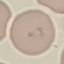
Summary:
  - Malaria status: uninfected
  - Preparation: thin smear
  - Capture: smartphone through the microscope eyepiece
  - Image type: cell patch, automatically extracted from a larger field of view and resized to 64 × 64 pixels
  - Stain: Giemsa